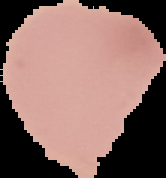
image type = cell region segmented out of the field of view; surrounding area masked to black
preparation = thin blood film
image size = 166×178 pixels
result = negative for Plasmodium parasites